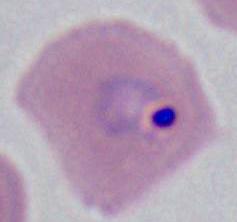
Micrograph. A Plasmodium parasite is shown. 400x or 1000x magnification.